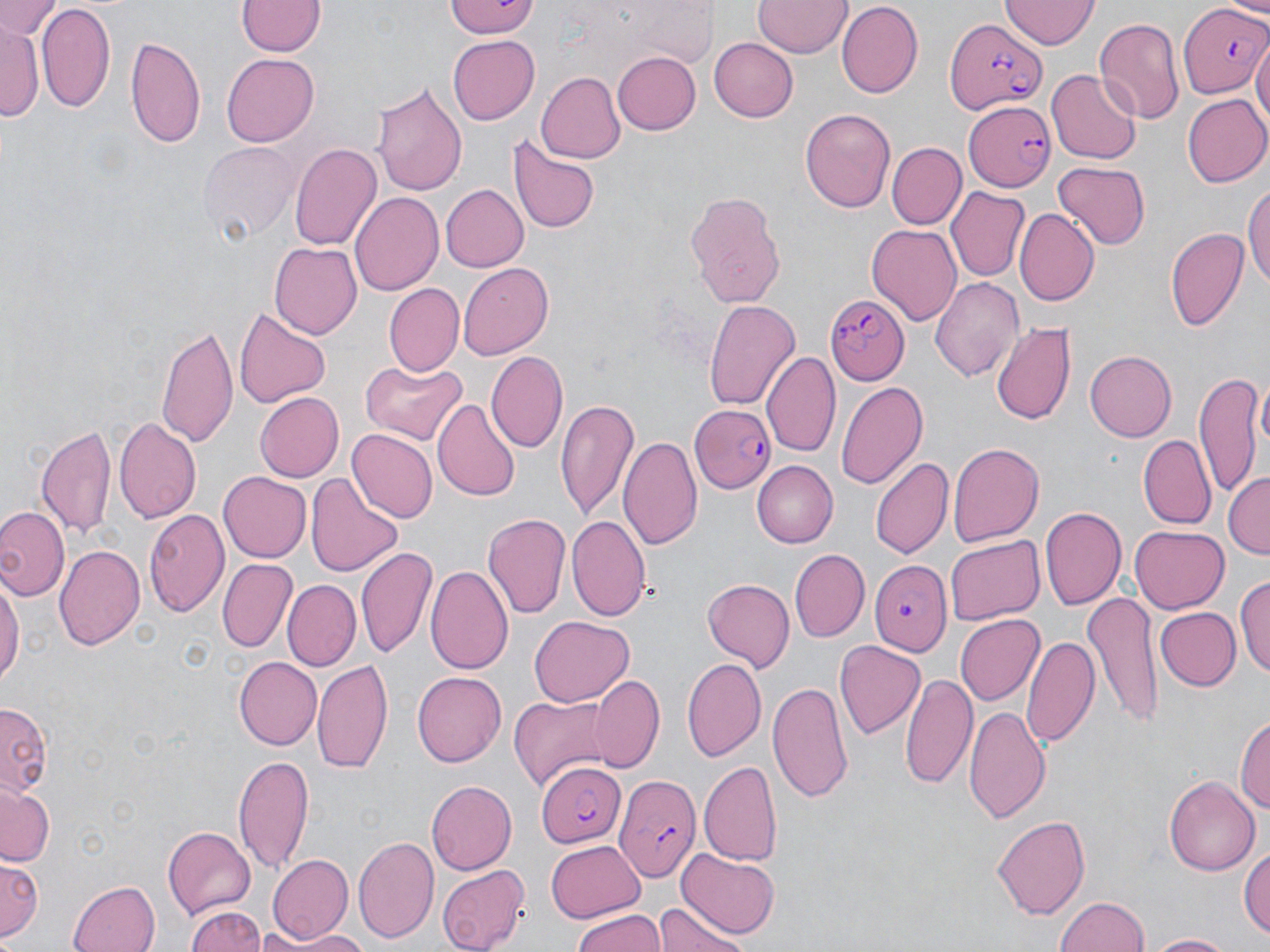

Summary:
  - Coordinate format: approximate bounding boxes as (x1, y1, x2, y2) in pixels
  - Uninfected red blood cell locations: (2, 0, 61, 43), (445, 0, 539, 39), (236, 1, 324, 58), (754, 1, 851, 59), (1000, 1, 1097, 50), (836, 3, 922, 97), (36, 4, 116, 115), (1094, 16, 1184, 127), (3, 22, 40, 122), (126, 34, 207, 151), (708, 35, 798, 120), (1253, 36, 1269, 139), (448, 37, 539, 123), (612, 49, 701, 134), (222, 54, 320, 146), (1046, 69, 1141, 164), (534, 72, 625, 164), (373, 78, 467, 198), (1183, 93, 1270, 187), (800, 107, 897, 213), (508, 134, 599, 235), (197, 138, 299, 242), (290, 141, 381, 252), (885, 142, 966, 230), (1051, 163, 1153, 249), (1243, 178, 1270, 293), (439, 183, 528, 272), (946, 187, 1029, 280), (685, 189, 787, 307), (351, 190, 444, 297), (1015, 209, 1099, 305), (865, 223, 962, 326), (1165, 226, 1248, 331), (269, 240, 363, 339), (457, 262, 554, 361), (931, 276, 1025, 384), (383, 283, 463, 377), (704, 298, 801, 411), (234, 305, 330, 408), (991, 318, 1076, 426), (156, 322, 240, 450), (487, 349, 568, 454), (1085, 351, 1177, 441), (762, 352, 841, 460), (358, 358, 467, 444), (1195, 371, 1267, 498), (835, 379, 929, 490), (254, 391, 343, 482), (433, 397, 523, 500), (556, 397, 639, 522), (114, 417, 201, 524), (37, 425, 118, 544), (347, 429, 438, 524), (619, 433, 703, 550), (1139, 436, 1214, 528), (946, 440, 1041, 547), (870, 455, 953, 560), (753, 462, 839, 547), (216, 471, 310, 562), (305, 473, 403, 578), (1225, 473, 1269, 559), (0, 506, 67, 600), (1040, 506, 1126, 612), (144, 508, 228, 618), (482, 511, 571, 619), (568, 517, 650, 621), (1130, 526, 1229, 614), (944, 535, 1042, 625), (357, 543, 437, 660), (55, 545, 146, 652), (789, 550, 869, 643), (217, 559, 295, 653), (426, 563, 513, 675), (0, 569, 22, 693), (1235, 572, 1269, 679), (702, 578, 795, 670), (282, 581, 361, 673), (1084, 593, 1163, 728), (1154, 605, 1240, 690), (954, 613, 1042, 706), (529, 615, 631, 708), (1023, 633, 1101, 751), (836, 640, 925, 741), (233, 656, 322, 751), (681, 657, 767, 763), (312, 659, 394, 773), (900, 669, 976, 790), (413, 670, 508, 768), (589, 674, 665, 774), (767, 680, 854, 802), (508, 694, 614, 788), (964, 703, 1050, 823), (0, 704, 52, 796), (1235, 710, 1270, 823), (232, 754, 316, 874), (698, 759, 782, 865), (1165, 774, 1260, 876), (426, 780, 514, 874), (0, 784, 53, 867), (992, 813, 1090, 921), (163, 826, 257, 917), (354, 835, 439, 944), (547, 840, 645, 920), (1242, 840, 1270, 943), (678, 848, 780, 936), (266, 852, 353, 945), (1, 857, 41, 944), (437, 864, 527, 951), (69, 878, 163, 952), (1054, 895, 1151, 952), (657, 898, 751, 952), (184, 903, 269, 952), (572, 907, 665, 952), (286, 932, 373, 952), (1144, 932, 1234, 951)
  - Plasmodium falciparum-infected red blood cell locations: (1179, 3, 1269, 99), (945, 17, 1049, 114), (964, 100, 1058, 191), (825, 294, 910, 386), (692, 406, 775, 495), (869, 559, 952, 656), (536, 760, 625, 848), (614, 774, 701, 881)
  - Slide-level diagnosis: Plasmodium falciparum
  - Magnification: 1000x
  - Stain: May-Grünwald-Giemsa
  - Field of view: one of a larger specimen
  - Image size: 1270×952 pixels
  - Preparation: thin blood smear
  - Modality: optical microscopy